Comment on the morphology of the erythrocytes.
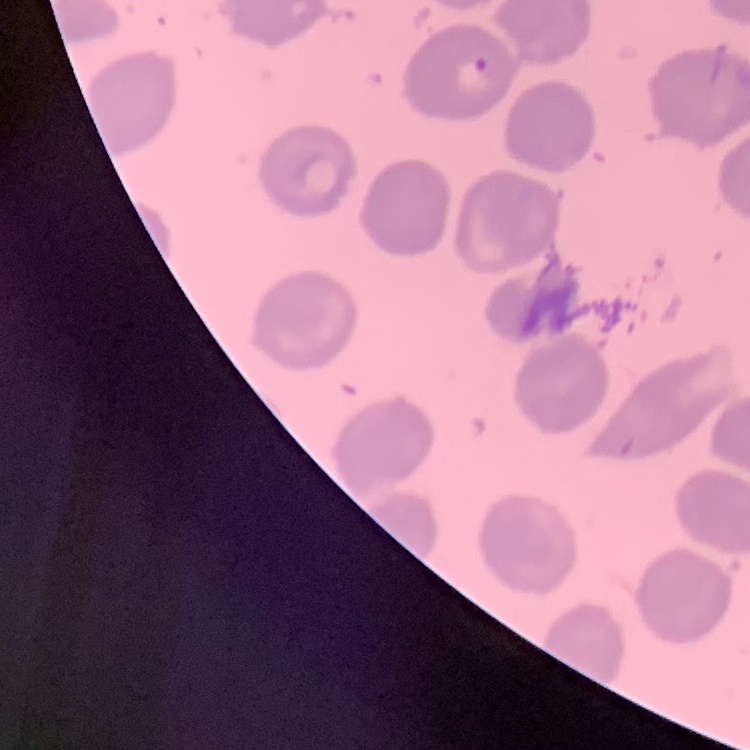

No rouleaux formation.

One tile cut from a larger photomicrograph. Stained with either Field's or Giemsa. Thin blood film.